Assess this cell for malaria.
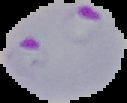
It is parasitized.

Summary:
  - Image size: 127×103 pixels
  - Image type: segmented cell region on a black background
  - Preparation: thin blood smear